Assess this cell for malaria.
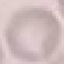
Uninfected.

Acquired by smartphone through the microscope eyepiece. Thin blood smear. Automatically extracted cell patch, resized to 64 × 64 pixels. Giemsa stain.